Identify the parasite.
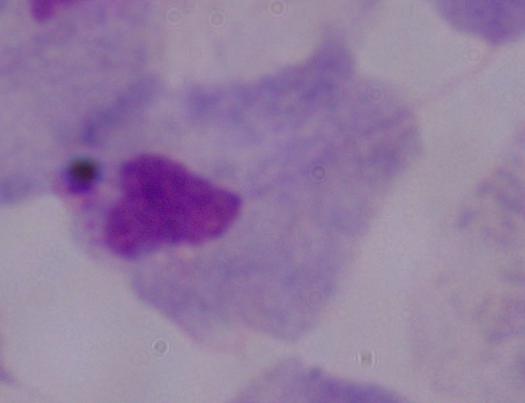
This is a trichomonad.

Summary:
  - Magnification: 1000x
  - Modality: photomicrograph